Report the malaria status of this cell.
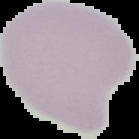

It is uninfected.

image type = segmented cell region with the area outside set to black
preparation = thin blood film
image size = 139×139 pixels